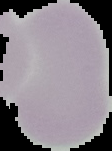
Malaria status: uninfected. Cell region segmented out of the field of view; the surrounding area is masked to black. From a thin blood film. Image is 112×151 pixels.